Mark where platelets are.
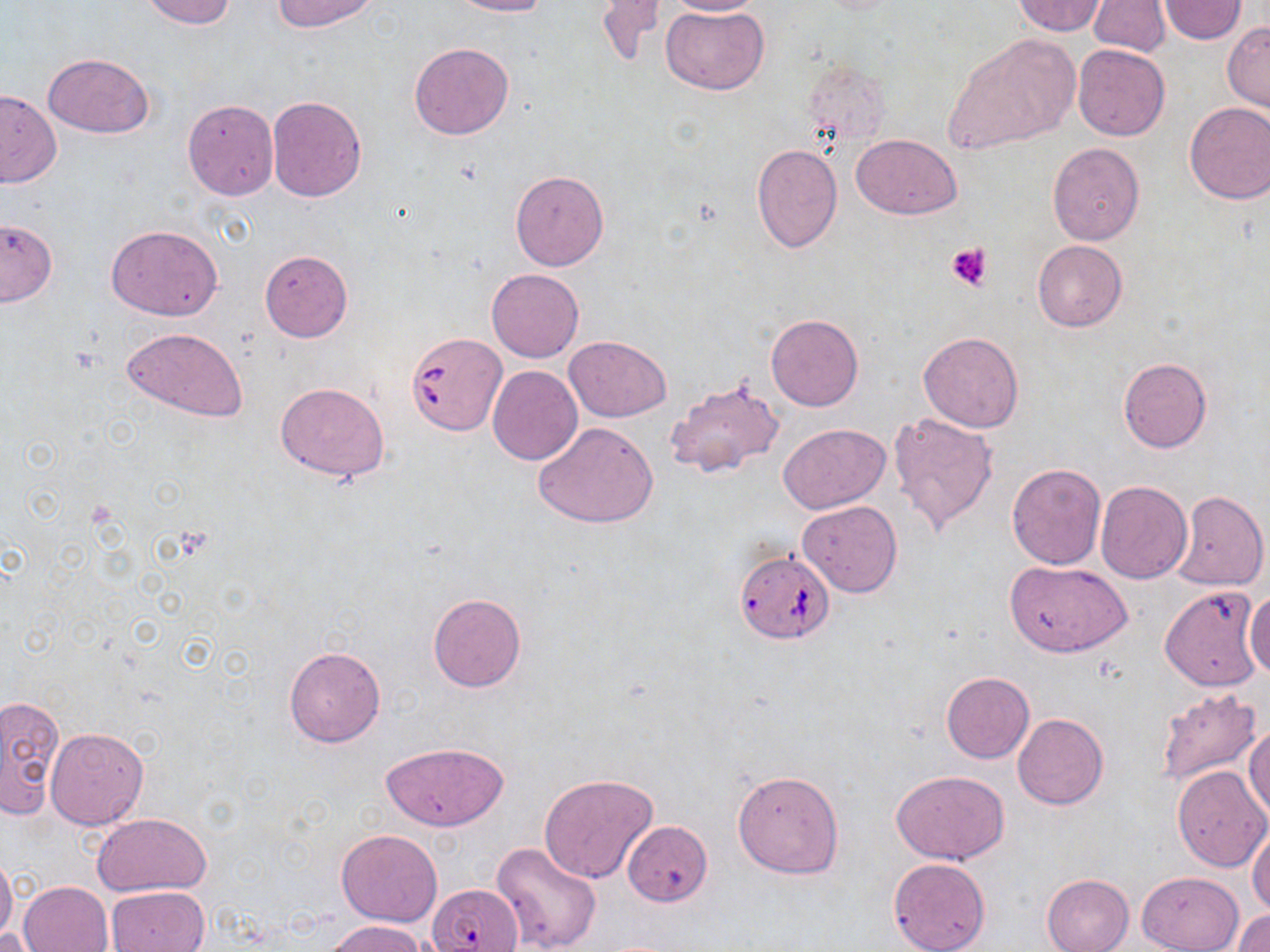
Approximate bounding boxes as (x1,y1)-(x2,y2) corner pairs in pixels.
Platelets: (946,241)-(995,291).

Summary:
  - Uninfected red blood cell locations: (140,0)-(235,28), (271,0)-(378,31), (448,0)-(552,17), (594,0)-(665,68), (666,0)-(768,16), (1013,1)-(1107,36), (1088,1)-(1172,57), (1158,1)-(1248,45), (661,4)-(769,95), (1222,22)-(1270,112), (943,32)-(1080,153), (408,42)-(515,140), (1073,44)-(1170,141), (43,52)-(155,137), (800,57)-(892,147), (0,89)-(62,188), (267,95)-(367,202), (182,100)-(278,200), (1184,101)-(1270,204), (852,134)-(961,219), (752,142)-(842,254), (1048,142)-(1145,244), (509,170)-(609,270), (0,218)-(58,306), (106,224)-(224,321), (1031,239)-(1127,330), (259,250)-(353,343), (486,268)-(584,362), (765,313)-(863,411), (120,327)-(247,422), (918,332)-(1024,432), (565,335)-(669,421), (1117,358)-(1212,453), (487,365)-(583,466), (666,374)-(784,481), (275,381)-(390,482), (887,411)-(1000,536), (532,420)-(660,528), (778,423)-(891,514), (1006,463)-(1105,569), (1096,481)-(1192,584), (1171,489)-(1268,591), (798,500)-(902,598), (1006,560)-(1133,657), (1245,585)-(1270,679), (1159,586)-(1264,692), (428,593)-(526,692), (284,646)-(386,747), (941,672)-(1033,763), (1153,687)-(1263,789), (0,694)-(64,819), (1012,713)-(1108,809), (1245,724)-(1270,821), (46,727)-(148,829), (381,742)-(509,832), (1171,766)-(1270,872), (733,768)-(844,878), (891,770)-(1009,865), (538,773)-(659,885), (92,812)-(212,895), (621,819)-(713,906), (1249,823)-(1270,916), (336,829)-(443,926), (491,840)-(604,952), (0,853)-(17,946), (888,858)-(991,952), (1137,872)-(1243,952), (1042,874)-(1134,952), (19,880)-(113,951), (426,882)-(519,952), (105,885)-(211,952), (1233,909)-(1270,951), (327,919)-(426,952), (0,923)-(43,951)
  - Babesia divergens-infected red blood cell locations: (405,331)-(509,435), (737,556)-(836,648)
  - Slide-level diagnosis: Babesia divergens
  - Magnification: 1000x
  - Field of view: single
  - Image size: 1270×952 pixels
  - Preparation: thin blood film
  - Modality: light microscopy
  - Stain: May-Grünwald-Giemsa